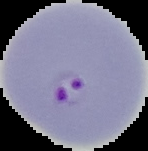
image size = 148×151 pixels
malaria status = parasitized
image type = segmented cell region with the area outside set to black
preparation = thin blood film